Assess this cell for malaria.
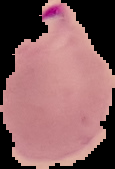
Parasitized.

image type = segmented cell region with the area outside set to black
preparation = thin blood film
image size = 115×169 pixels